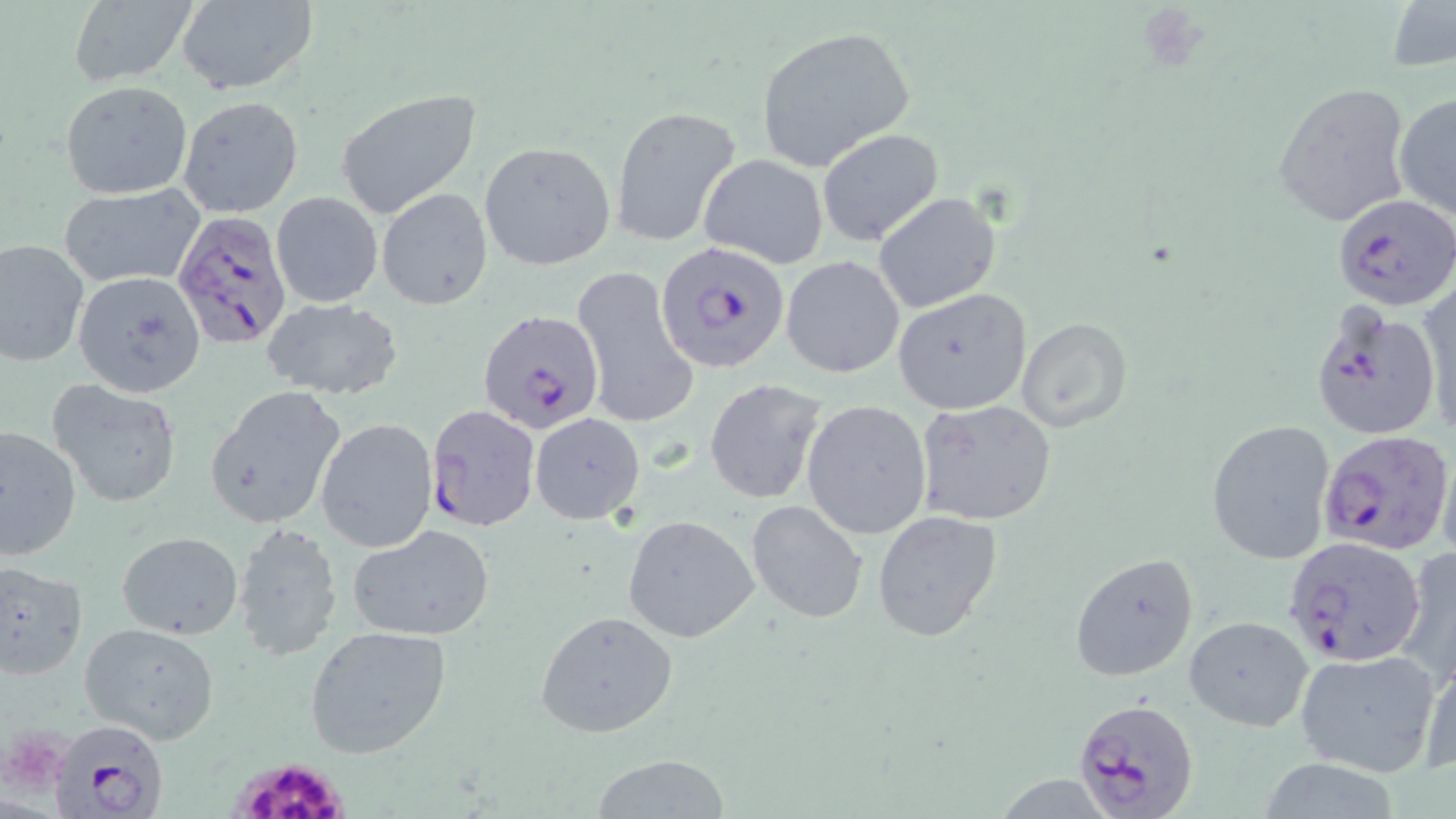

Approximate bounding boxes as (x1,y1)-(x2,y2) corner pairs in pixels. Plasmodium falciparum-infected red blood cell locations: (1332,193)-(1455,311), (172,208)-(292,353), (654,241)-(788,374), (1309,300)-(1443,445), (478,310)-(602,434), (424,404)-(541,531), (1318,429)-(1452,556), (1284,536)-(1427,667), (1072,696)-(1200,818), (48,719)-(166,819). Platelet locations: (226,753)-(352,819). Uninfected red blood cell locations: (1387,0)-(1456,75), (173,1)-(319,95), (66,2)-(198,87), (754,26)-(917,170), (60,81)-(192,200), (1271,82)-(1414,228), (334,89)-(482,220), (1393,92)-(1456,223), (177,95)-(303,217), (610,105)-(740,247), (816,127)-(945,247), (479,140)-(616,271), (699,154)-(829,269), (60,185)-(205,287), (377,187)-(493,310), (270,191)-(383,310), (872,192)-(1001,314), (0,239)-(89,367), (781,255)-(905,379), (571,264)-(696,428), (74,271)-(206,398), (1416,281)-(1455,439), (892,288)-(1033,415), (261,297)-(405,402), (1013,318)-(1132,432), (704,378)-(827,504), (47,379)-(185,508), (204,386)-(346,528), (915,398)-(1059,527), (802,400)-(933,540), (529,412)-(645,525), (316,417)-(438,552), (1206,420)-(1334,565), (1,426)-(80,560), (746,499)-(868,624), (872,511)-(1003,644), (622,515)-(760,644), (232,523)-(341,662), (348,525)-(497,642), (116,531)-(243,640), (1393,545)-(1456,684), (1068,553)-(1200,681), (0,559)-(88,680), (535,611)-(680,738), (1183,616)-(1313,732), (79,621)-(222,743), (305,624)-(453,761), (1417,647)-(1456,777), (1294,648)-(1441,776), (590,755)-(735,817). Slide-level diagnosis: Plasmodium falciparum. May-Grünwald-Giemsa stain. Light microscopy. 1000x magnification. Image is 1456×819 pixels. One field of a larger specimen. Thin blood smear.